Assess this cell for malaria.
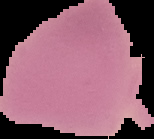

It is uninfected.

image type = segmented cell region on a black background
preparation = thin blood film
image size = 154×139 pixels